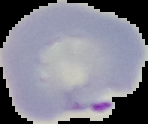
Summary:
  - Malaria status: parasitized
  - Image size: 148×124 pixels
  - Image type: cell region segmented out of the field of view; surrounding area masked to black
  - Preparation: thin blood smear